Assess the morphology of the erythrocytes.
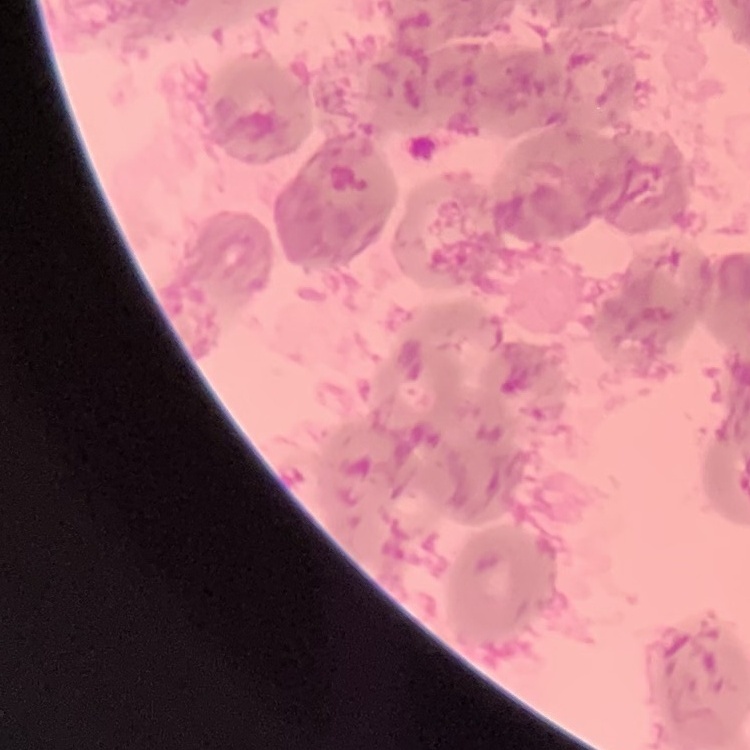

Rouleaux formation.

{
  "stain": "Field's or Giemsa",
  "preparation": "thin blood film",
  "image_type": "one tile cut from a larger photomicrograph"
}